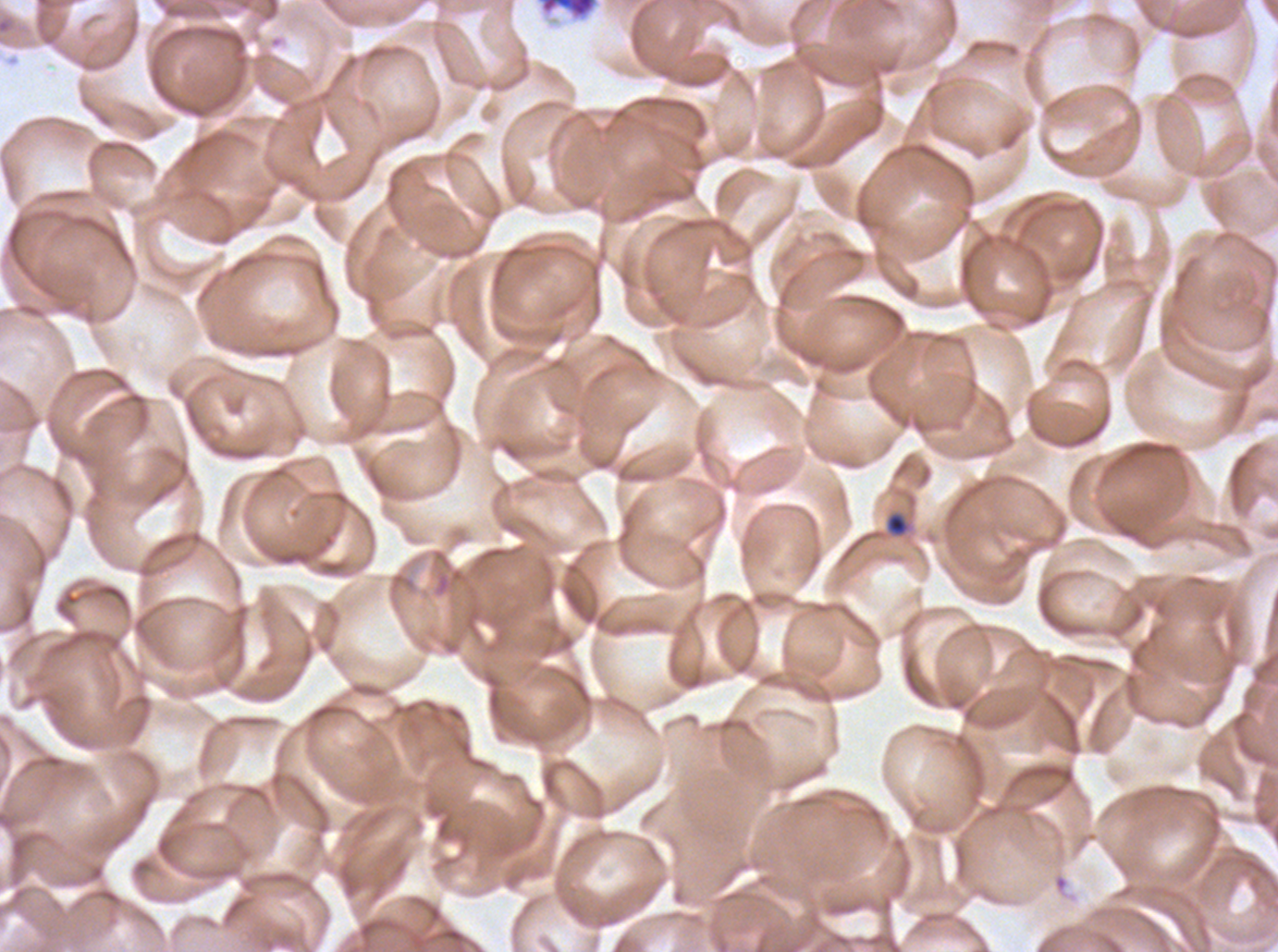
{
  "field_of_view": "one sub-image of a larger composite",
  "image_size": "1278×952 pixels",
  "debris_locations": "approximate bounding rectangles given as corner coordinates in pixels from the top-left: (x1=535, y1=0, x2=601, y2=23)",
  "stain": "Giemsa",
  "late_ring_early_trophozoite_locations": "approximate bounding rectangles given as corner coordinates in pixels from the top-left: (x1=885, y1=511, x2=910, y2=537)",
  "preparation": "thin blood film",
  "specimen": "Plasmodium falciparum cultured ex vivo for 24 to 48 hours, from a patient in The Gambia"
}